State which cell type is depicted.
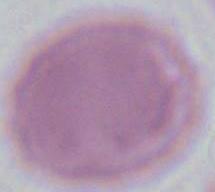

An erythrocyte.

magnification = 1000x
modality = photomicrograph